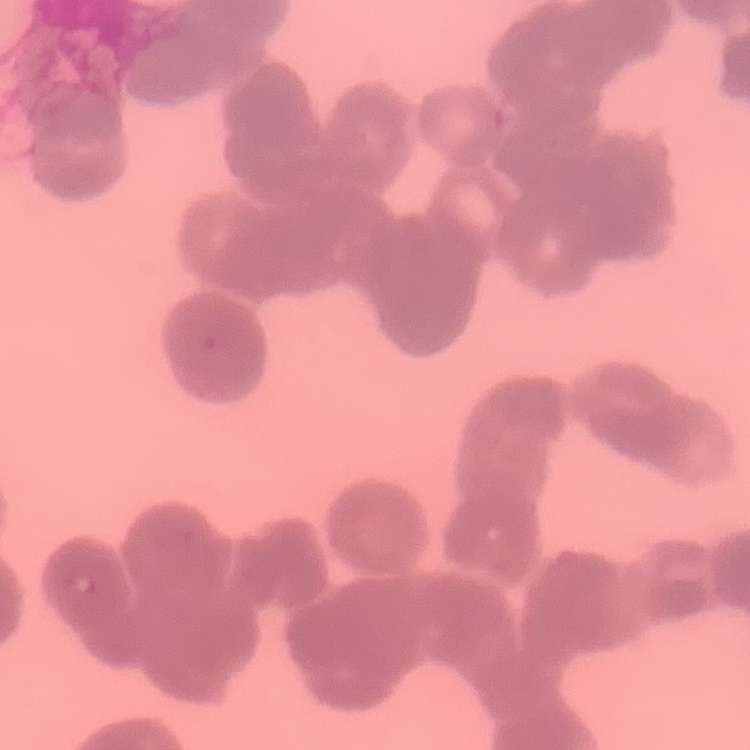

red_blood_cell_morphology: rouleaux formation
stain: Field's or Giemsa
image_type: one tile cut from a larger photomicrograph
preparation: thin peripheral smear